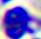
A white blood cell is seen. Photomicrograph. Captured at 400x magnification.